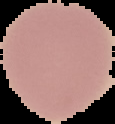

result: negative for Plasmodium parasites
preparation: thin blood film
image_type: segmented cell region on a black background
image_size: 115×124 pixels